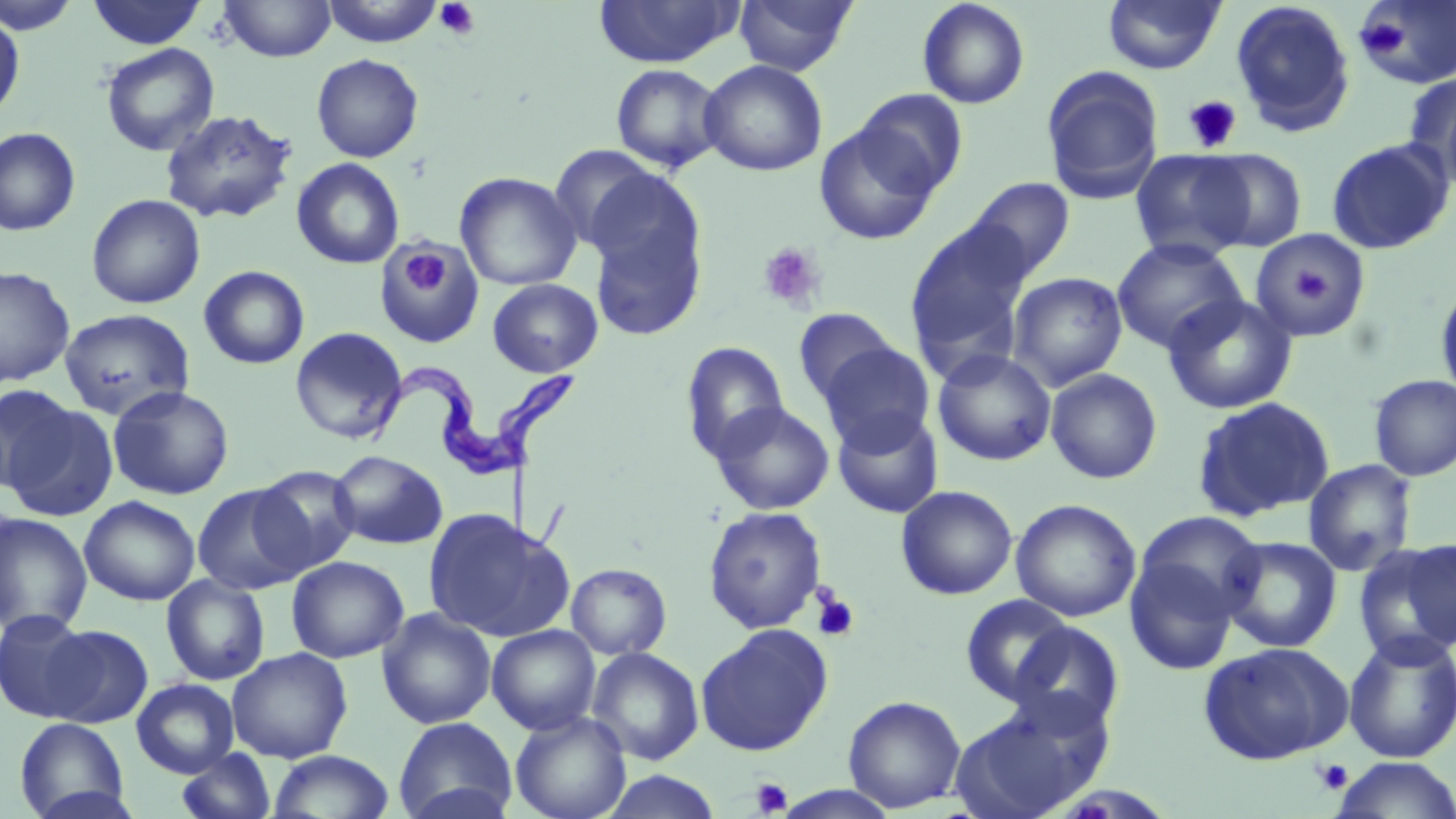
Summary:
  - Coordinate format: approximate bounding boxes as (x1,y1)-(x2,y2) corner pairs in pixels
  - Trypanosoma brucei locations: (369,350)-(582,483)
  - Uninfected red blood cell locations: (0,0)-(81,35), (87,0)-(207,49), (220,0)-(337,62), (320,0)-(445,47), (734,0)-(857,76), (917,0)-(1030,109), (1355,0)-(1456,89), (594,1)-(741,67), (1103,1)-(1225,74), (1230,1)-(1357,137), (0,13)-(25,120), (100,43)-(219,157), (311,53)-(424,162), (699,59)-(828,177), (610,64)-(725,173), (1041,65)-(1164,205), (1401,72)-(1456,181), (1439,87)-(1456,198), (855,89)-(968,198), (159,109)-(297,224), (814,120)-(943,245), (0,127)-(81,236), (1326,138)-(1454,255), (548,144)-(663,252), (1130,149)-(1255,262), (1196,149)-(1308,253), (291,158)-(405,269), (454,171)-(582,290), (966,177)-(1076,281), (586,182)-(708,341), (86,194)-(206,309), (905,221)-(1035,375), (1250,230)-(1373,342), (1111,237)-(1247,353), (375,244)-(484,348), (0,265)-(75,387), (198,265)-(310,369), (1006,271)-(1128,391), (487,278)-(603,378), (1434,279)-(1456,404), (1163,293)-(1298,415), (59,308)-(194,420), (793,308)-(901,407), (289,327)-(409,444), (680,341)-(789,462), (819,343)-(935,453), (933,349)-(1056,466), (1045,368)-(1163,484), (1369,374)-(1456,481), (0,384)-(77,494), (107,385)-(234,500), (1191,396)-(1336,522), (4,400)-(119,522), (709,401)-(835,515), (832,408)-(943,519), (329,450)-(448,549), (1303,459)-(1418,577), (252,465)-(361,575), (192,483)-(309,595), (895,485)-(1018,600), (79,495)-(201,606), (1010,498)-(1141,622), (703,506)-(827,634), (423,508)-(573,642), (1134,511)-(1266,620), (0,512)-(93,635), (1219,535)-(1342,653), (1378,537)-(1456,658), (1124,555)-(1240,675), (286,556)-(409,663), (566,563)-(672,660), (162,574)-(270,686), (959,594)-(1075,704), (376,608)-(496,729), (0,610)-(94,722), (1006,621)-(1126,733), (694,623)-(834,756), (42,624)-(153,728), (487,624)-(601,735), (1341,630)-(1456,764), (1198,641)-(1353,764), (587,646)-(704,764), (227,648)-(353,763), (131,678)-(239,778), (843,695)-(966,813), (951,695)-(1110,819), (510,710)-(631,819), (394,716)-(516,819), (14,717)-(130,819), (175,748)-(277,819), (267,749)-(395,818), (1330,757)-(1456,818), (600,771)-(724,818), (772,786)-(901,819)
  - Platelet locations: (434,1)-(480,40), (1355,17)-(1410,60), (1183,95)-(1242,153), (757,241)-(827,314), (400,246)-(451,297), (1292,270)-(1330,303), (812,590)-(860,643), (1312,758)-(1354,795), (750,777)-(792,816)
  - Slide-level diagnosis: Trypanosoma brucei
  - Preparation: thin blood film
  - Magnification: 1000x
  - Modality: optical microscopy
  - Field of view: single
  - Stain: May-Grünwald-Giemsa
  - Image size: 1456×819 pixels